Identify the parasite.
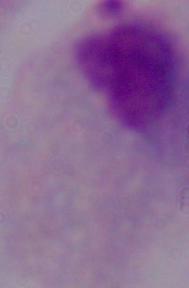
A trichomonad.

modality = photomicrograph
magnification = 1000x